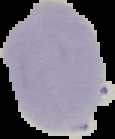

image type = segmented cell region on a black background
preparation = thin blood film
malaria status = uninfected
image size = 115×139 pixels